Classify this cell by malaria status.
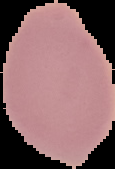

Uninfected.

image_size: 115×169 pixels
image_type: segmented cell region with the area outside set to black
preparation: thin blood film